Give the position of every leukocyte visible.
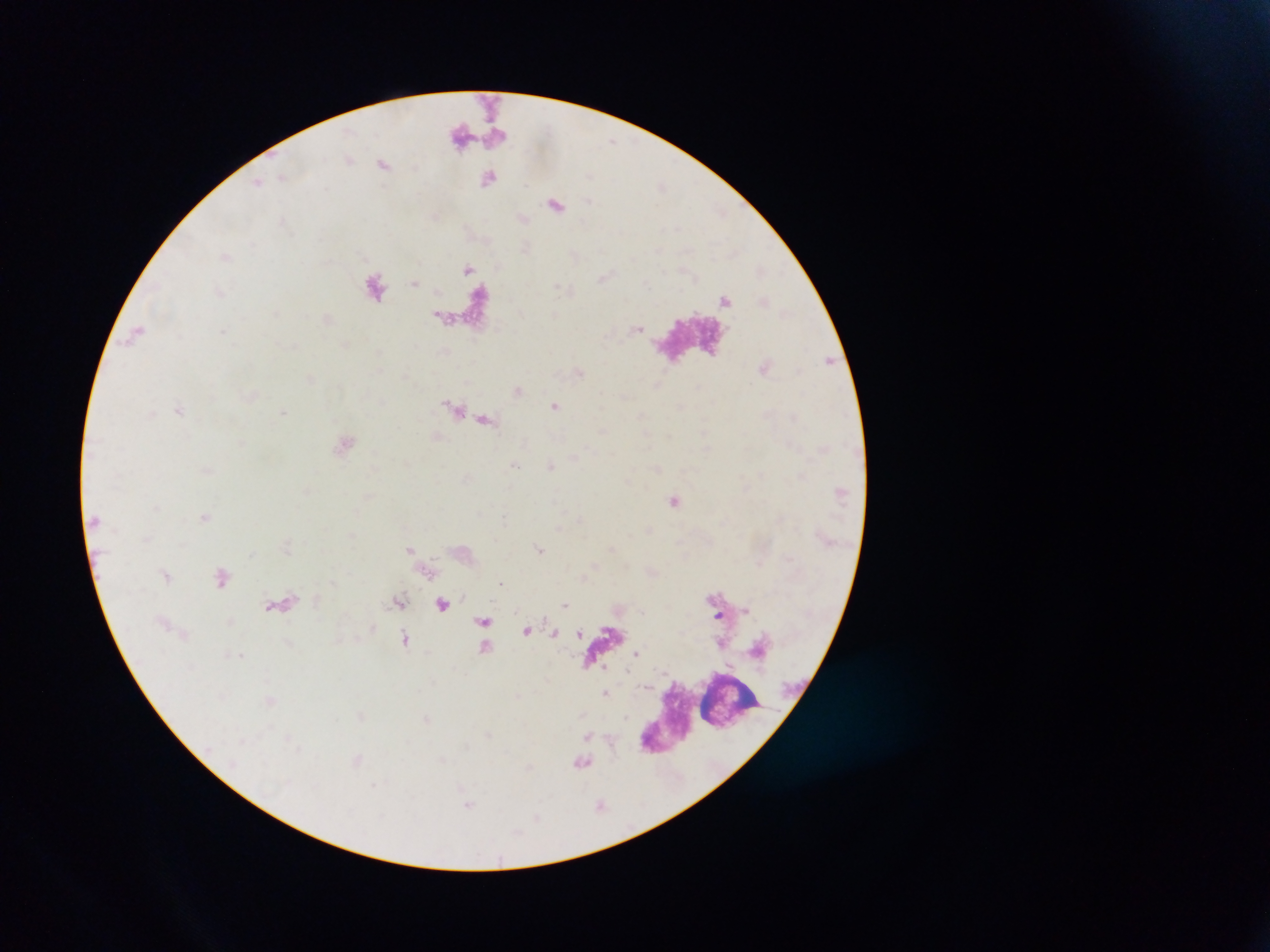

No leukocytes observed.

Approximate centers as (x, y) in pixels. Malaria parasite locations: (523, 218), (603, 277), (639, 328), (828, 358), (518, 390), (555, 405), (282, 413), (674, 501), (205, 515), (409, 549), (540, 549), (502, 582), (463, 597), (714, 597), (566, 605), (746, 610), (543, 616), (719, 617), (527, 630), (553, 633), (577, 633), (638, 653), (240, 654), (605, 668), (627, 672), (607, 693), (626, 717), (587, 736). Thick blood smear. Mobile-phone photograph taken through the microscope. Image is 1270×952 pixels. One field of view. Collected in Ghana.